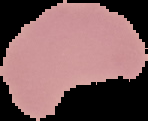

image type = segmented cell region with the area outside set to black
result = malaria parasites detected
image size = 148×121 pixels
preparation = thin blood smear